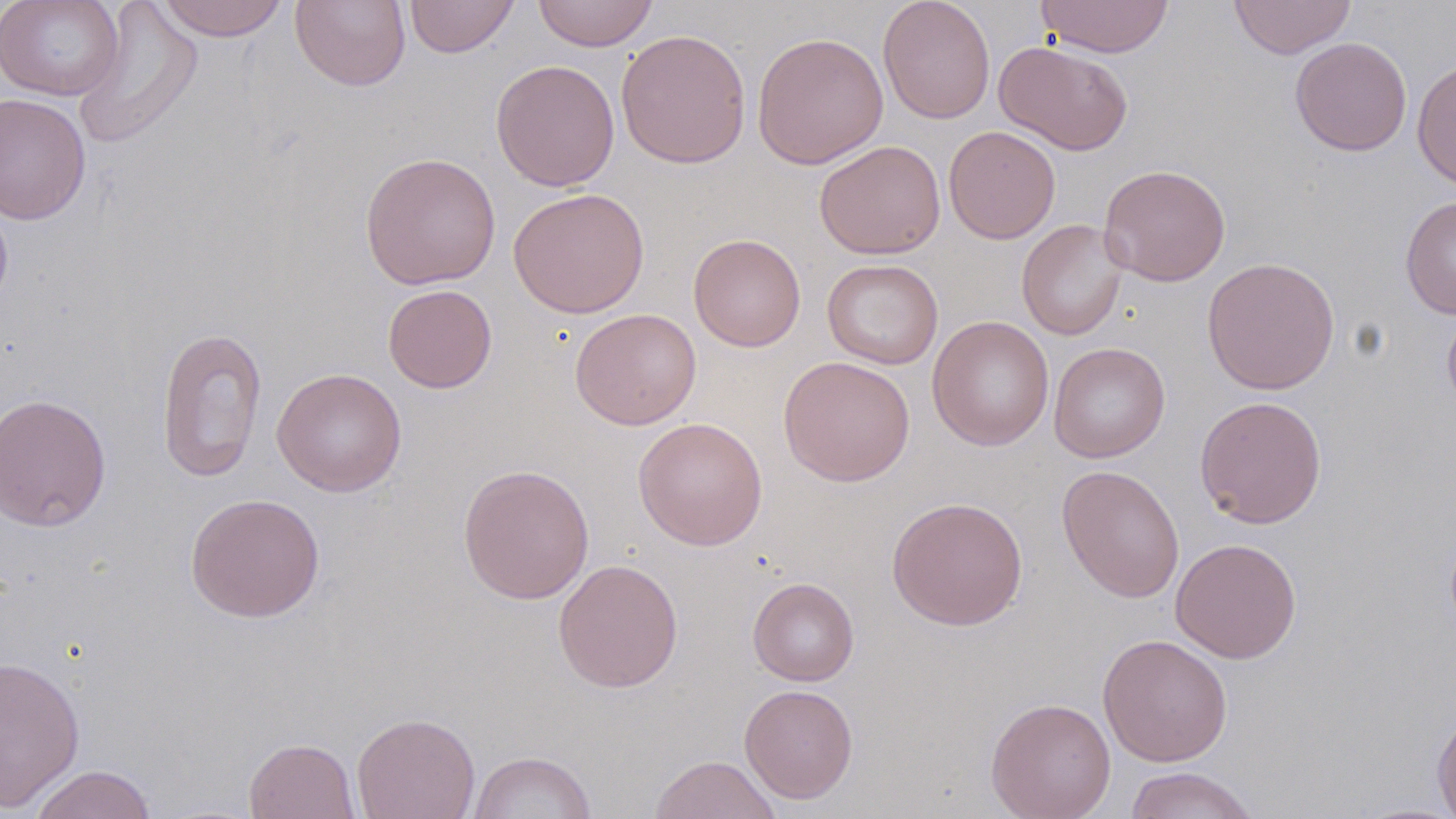 Approximate bounding boxes as [x1, y1, x2, y2] in pixels. Uninfected red blood cell locations: [0, 0, 125, 101], [154, 0, 290, 41], [405, 0, 519, 57], [531, 0, 658, 52], [878, 0, 996, 125], [1037, 0, 1174, 58], [1228, 0, 1356, 59], [72, 1, 204, 150], [290, 1, 411, 91], [615, 28, 752, 169], [751, 31, 889, 169], [1289, 36, 1412, 157], [994, 40, 1133, 155], [1412, 57, 1456, 192], [490, 59, 620, 191], [0, 92, 92, 225], [943, 125, 1061, 244], [814, 140, 945, 259], [359, 151, 501, 290], [1098, 164, 1230, 287], [508, 188, 649, 318], [0, 193, 13, 315], [1399, 194, 1456, 319], [1016, 219, 1129, 341], [688, 233, 806, 352], [1201, 256, 1340, 395], [822, 258, 944, 370], [382, 284, 497, 393], [1442, 302, 1456, 414], [570, 308, 701, 430], [927, 316, 1054, 451], [156, 325, 267, 484], [1048, 342, 1170, 462], [778, 355, 915, 487], [271, 367, 407, 496], [0, 392, 112, 532], [1194, 395, 1328, 529], [632, 416, 768, 551], [457, 463, 595, 603], [1056, 465, 1185, 603], [185, 493, 326, 622], [886, 496, 1028, 631], [1170, 538, 1302, 664], [553, 558, 683, 692], [748, 577, 859, 686], [1097, 633, 1233, 767], [0, 655, 85, 811], [739, 684, 858, 803], [985, 697, 1116, 819], [1431, 708, 1456, 819], [351, 712, 480, 819], [243, 737, 361, 819], [468, 751, 597, 818], [649, 754, 782, 818], [28, 765, 157, 819], [1123, 767, 1261, 819], [1351, 801, 1456, 818]. Slide-level diagnosis: no evidence of blood parasites. Image is 1456×819 pixels. May-Grünwald-Giemsa-stained preparation. Thin blood film. Single field of view. Optical microscopy. 1000x magnification.